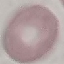

Malaria status: uninfected. Giemsa stain. Thin smear of blood. Automatically extracted cell patch, resized to 64 × 64 pixels. Acquired by smartphone through the microscope eyepiece.